Outline every Plasmodium parasite.
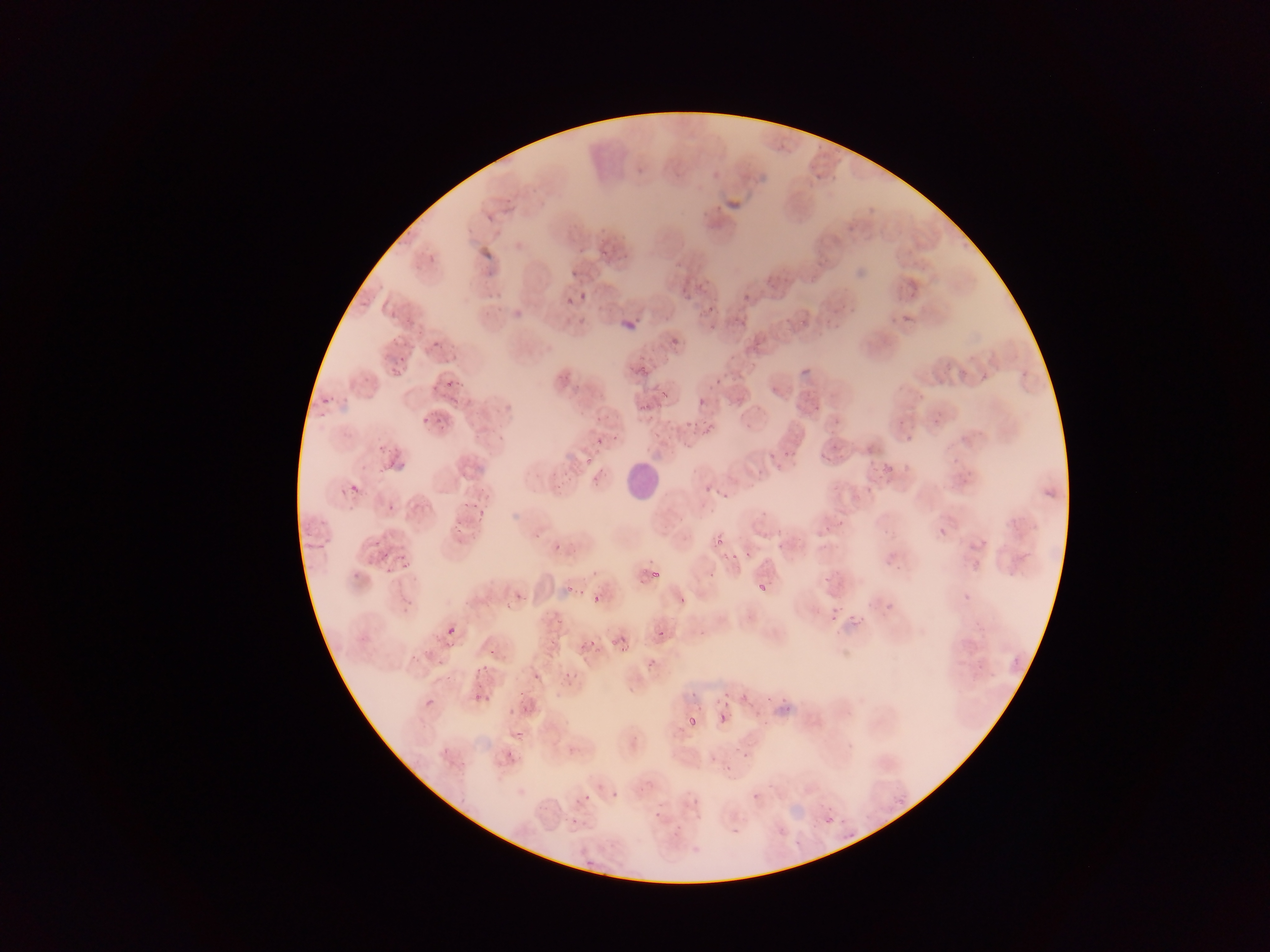

Approximate bounding boxes as left top right bottom in pixels.
Plasmodium parasites (some below the resolvable threshold): 603 242 613 259; 483 253 497 259; 571 269 579 277; 679 288 691 300; 743 290 757 301; 580 293 587 302; 709 306 716 314; 625 312 650 330; 905 315 914 324; 665 340 677 347; 431 342 441 350; 388 352 404 377; 797 361 817 380; 632 366 645 376; 445 371 466 387; 714 378 723 386; 659 385 676 398; 428 386 439 393; 320 397 328 405; 697 398 704 407; 635 399 650 411; 809 403 820 409; 421 412 433 423; 704 417 722 435; 684 420 693 427; 906 436 914 444; 374 437 386 457; 594 437 602 446; 785 437 804 459; 827 442 850 462; 757 446 778 467; 379 459 396 478; 701 476 718 496; 347 484 362 496; 866 485 873 493; 717 488 729 496; 462 493 483 510; 385 503 393 508; 819 519 836 531; 938 528 948 538; 714 536 724 546; 821 537 837 549; 378 539 396 554; 553 541 565 555; 778 542 785 550; 725 549 739 559; 741 551 755 559; 392 556 406 573; 822 569 840 586; 651 571 661 580; 566 582 578 597; 758 584 767 592; 678 593 690 606; 593 594 601 603; 879 598 894 612; 502 603 511 609; 827 613 837 626; 850 615 856 623; 857 621 862 630; 446 625 456 636; 575 628 607 664; 544 631 562 644; 655 633 663 642; 603 635 615 645; 445 638 457 652; 620 640 634 652; 486 649 500 660; 646 653 660 670; 432 656 445 664; 564 664 579 678; 731 686 745 705; 686 688 696 698; 474 693 486 703; 717 693 729 703; 752 695 769 709; 424 697 435 708; 519 697 530 708; 718 712 728 725; 688 715 696 725; 514 718 534 735; 501 745 528 777; 441 748 450 758; 723 759 738 780; 611 791 619 800; 748 793 772 814; 581 794 590 804; 694 799 704 809; 650 805 662 822; 821 816 838 828; 776 826 788 837 | approximate x y pixel centers of objects too small to bound: 457 529; 404 592.

Leukocyte locations: 622 459 660 500. Thin blood film. Mobile-phone photograph taken through the microscope. Collected in Ghana. Image is 1270×952 pixels. One field of view.